Name the cell type shown.
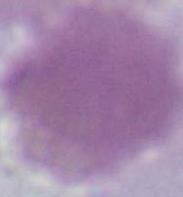

This is an erythrocyte.

Photomicrograph. 1000x magnification.